Classify this cell by malaria status.
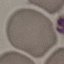

It is uninfected.

image type = automatically extracted cell patch, resized to 64 × 64 pixels
stain = Giemsa
preparation = thin blood smear
capture = smartphone through the microscope eyepiece